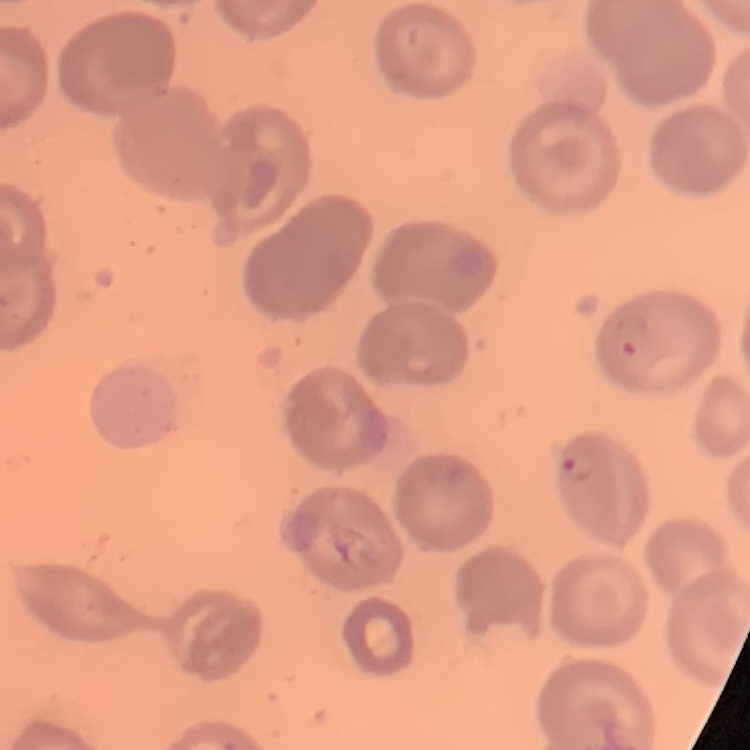
{
  "erythrocyte_morphology": "no rouleaux formation",
  "preparation": "thin blood film",
  "stain": "Field's or Giemsa",
  "image_type": "square crop of a larger photomicrograph"
}